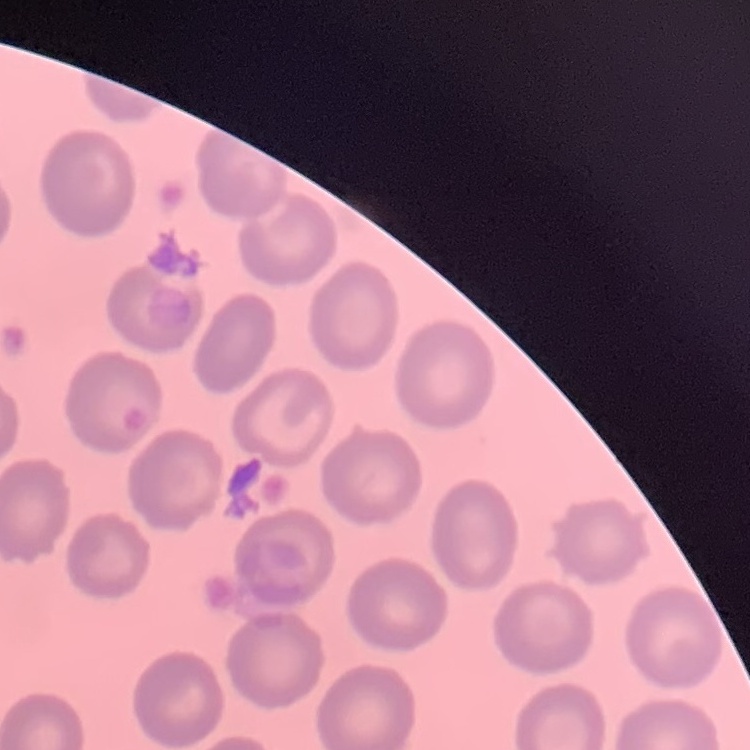 The erythrocytes exhibit no rouleaux formation. Stained with either Field's or Giemsa. Thin blood film. Square crop of a larger photomicrograph.